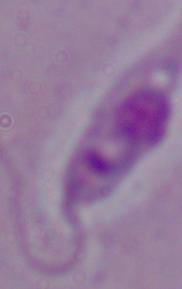
Summary:
  - Identification: Leishmania
  - Magnification: 1000x
  - Modality: micrograph